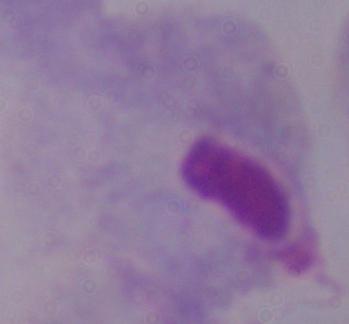

Summary:
  - Magnification: 1000x
  - Identification: trichomonad
  - Modality: micrograph